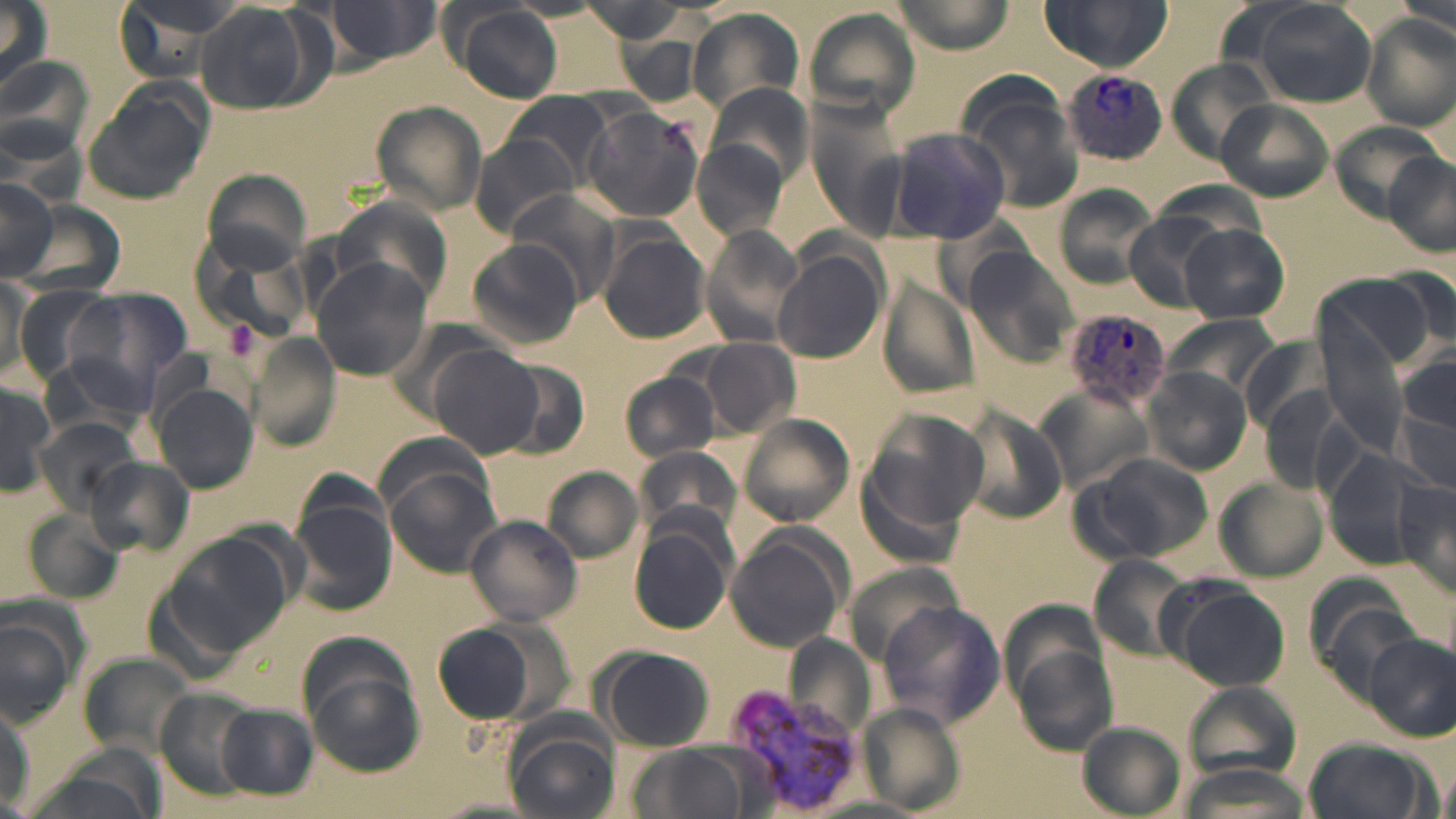
Summary:
  - Coordinate format: approximate bounding boxes as (x1,y1)-(x2,y2) corner pairs in pixels
  - Uninfected red blood cell locations: (1,0)-(53,95), (110,0)-(243,84), (312,0)-(445,65), (894,0)-(1018,52), (1040,0)-(1173,71), (1387,0)-(1454,40), (192,2)-(331,116), (1248,2)-(1378,109), (441,3)-(566,104), (805,7)-(917,119), (685,8)-(807,115), (1363,14)-(1455,128), (616,34)-(708,104), (0,54)-(95,164), (1165,57)-(1277,165), (957,78)-(1087,214), (702,82)-(814,192), (82,84)-(210,203), (502,92)-(616,189), (1217,99)-(1334,202), (370,100)-(489,217), (581,106)-(704,223), (4,118)-(86,210), (1329,121)-(1445,219), (887,126)-(1011,244), (471,133)-(587,237), (692,141)-(788,242), (1383,151)-(1456,255), (199,169)-(313,277), (0,178)-(60,280), (1054,186)-(1158,288), (505,189)-(621,305), (333,197)-(453,306), (8,200)-(128,298), (1123,213)-(1224,310), (698,224)-(803,348), (1180,224)-(1291,325), (598,229)-(712,344), (466,240)-(586,351), (773,248)-(886,364), (967,249)-(1077,365), (311,257)-(434,382), (1385,264)-(1456,357), (1322,273)-(1430,372), (1,279)-(39,383), (879,283)-(979,402), (12,286)-(109,381), (69,289)-(192,395), (1318,311)-(1405,456), (1166,314)-(1277,398), (248,337)-(341,450), (1243,337)-(1326,429), (701,338)-(800,436), (428,344)-(542,459), (496,357)-(589,459), (1397,357)-(1456,499), (1141,368)-(1251,476), (620,370)-(721,461), (0,376)-(54,498), (153,385)-(259,493), (959,406)-(1067,527), (857,409)-(984,559), (736,413)-(855,527), (35,417)-(139,514), (632,445)-(744,540), (1322,445)-(1437,565), (1073,450)-(1213,564), (87,456)-(190,555), (542,466)-(643,564), (385,470)-(500,578), (1393,477)-(1456,598), (1215,478)-(1326,582), (289,498)-(397,618), (22,511)-(123,607), (465,515)-(581,627), (628,523)-(734,636), (725,530)-(850,652), (162,532)-(295,658), (1090,554)-(1192,657), (1166,582)-(1290,691), (0,600)-(85,725), (879,602)-(1003,728), (431,620)-(547,727), (1366,635)-(1453,738), (1011,639)-(1117,755), (598,648)-(716,751), (81,652)-(191,758), (304,671)-(425,777), (1185,681)-(1303,780), (156,689)-(260,796), (859,703)-(965,814), (218,706)-(316,797), (505,715)-(619,819), (1080,722)-(1185,816), (1302,737)-(1429,819), (629,743)-(749,819)
  - Plasmodium vivax-infected red blood cell locations: (1063,70)-(1170,165), (1061,307)-(1173,410), (722,679)-(866,817)
  - Platelet locations: (221,318)-(261,365)
  - Slide-level diagnosis: Plasmodium vivax
  - Modality: optical microscopy
  - Magnification: 1000x
  - Image size: 1456×819 pixels
  - Stain: May-Grünwald-Giemsa
  - Field of view: one of a larger specimen
  - Preparation: thin blood smear